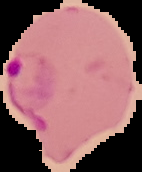
image size = 142×172 pixels
preparation = thin blood film
image type = segmented cell region with the area outside set to black
result = Plasmodium parasites detected